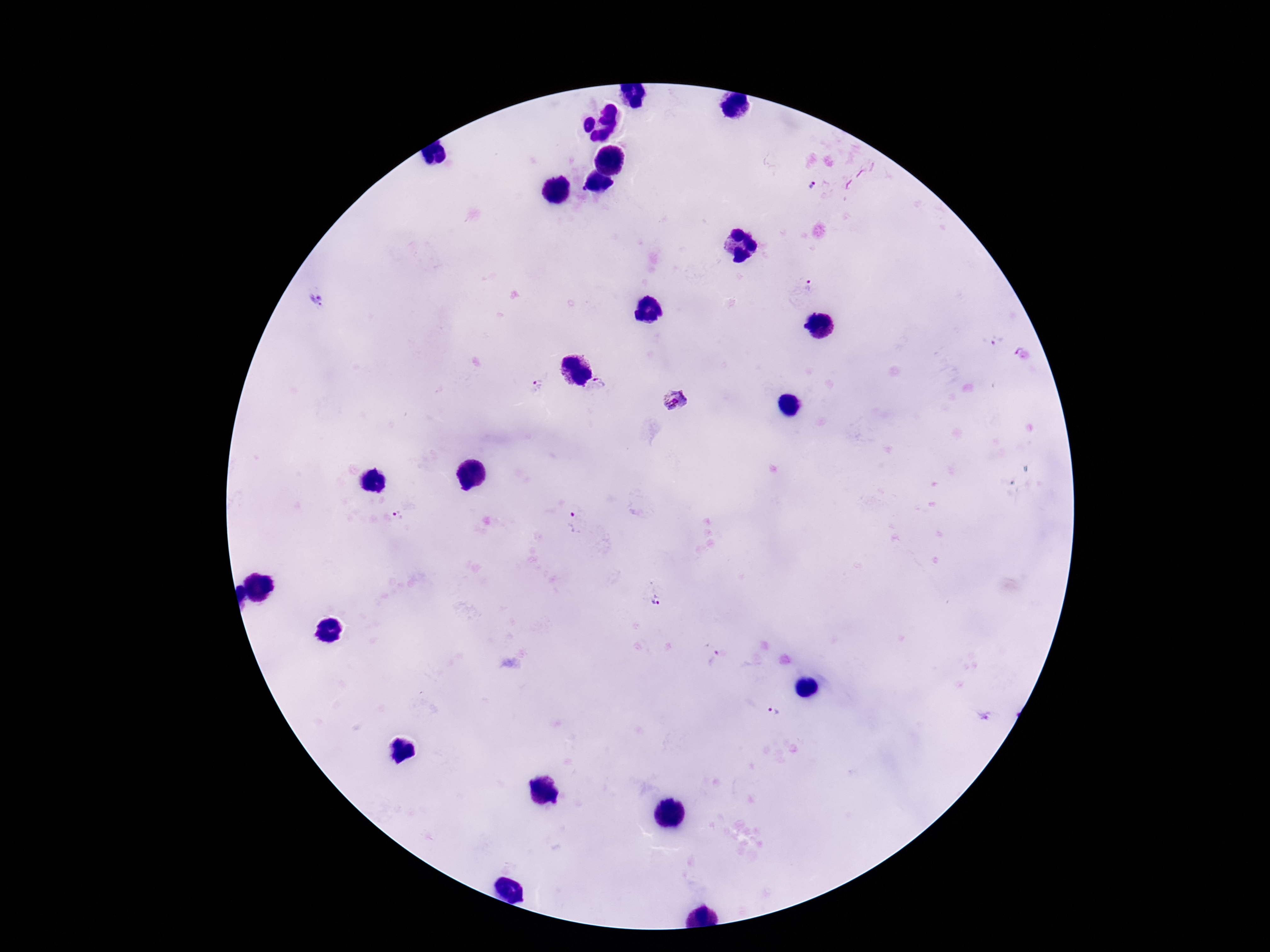
Approximate centers as {x, y} in pixels. Plasmodium parasite locations: {812, 187}, {811, 286}, {321, 302}, {998, 341}, {599, 385}, {537, 386}, {674, 400}, {401, 515}, {577, 525}, {655, 594}, {716, 660}, {774, 712}. Giemsa stain. Image is 1270×952 pixels. Single field of view. Thick blood smear. Patient malaria status: positive. 100x magnification. Photographed through the microscope eyepiece with a smartphone camera.